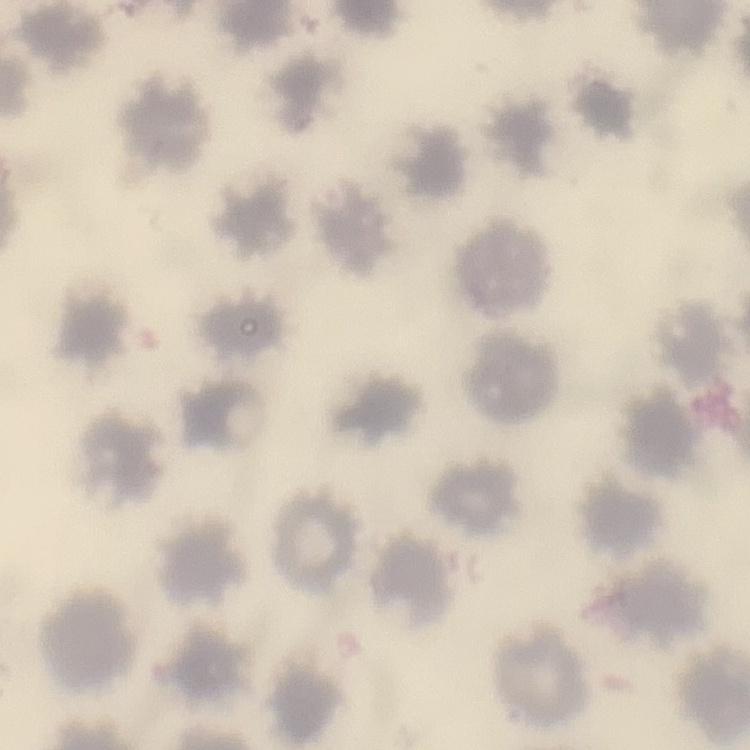

The red blood cells show no rouleaux formation. Square crop of a larger photomicrograph. Field's or Giemsa stain. Thin blood film.